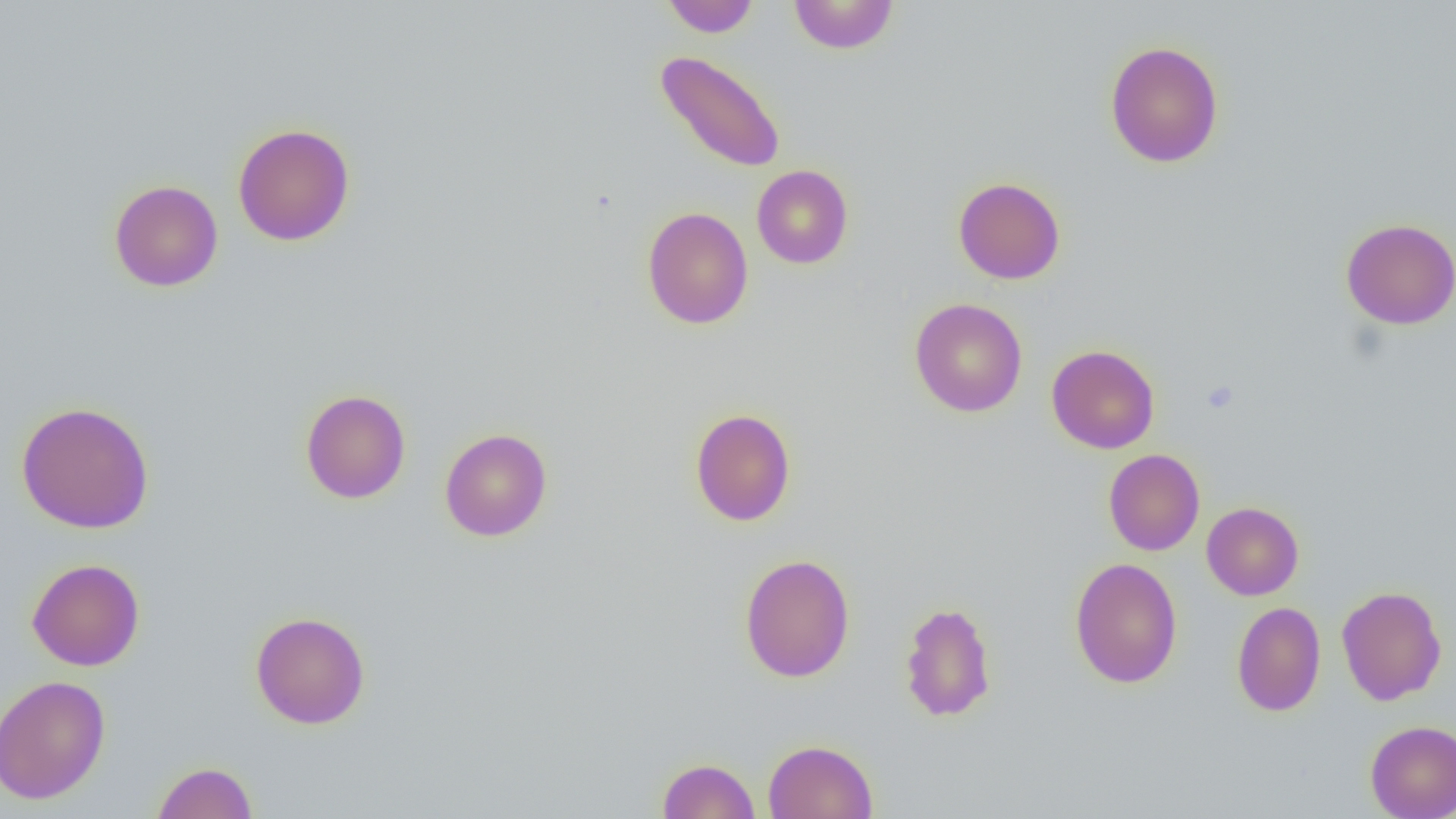 Approximate bounding boxes as named x1/y1/x2/y2 corners in pixels. Platelet locations: (x1=1201, y1=380, x2=1238, y2=413). Uninfected red blood cell locations: (x1=661, y1=0, x2=760, y2=37), (x1=788, y1=0, x2=900, y2=55), (x1=1104, y1=40, x2=1224, y2=168), (x1=654, y1=50, x2=786, y2=173), (x1=232, y1=123, x2=356, y2=246), (x1=751, y1=165, x2=853, y2=268), (x1=953, y1=177, x2=1066, y2=284), (x1=109, y1=179, x2=224, y2=292), (x1=641, y1=206, x2=754, y2=329), (x1=1340, y1=218, x2=1456, y2=330), (x1=909, y1=298, x2=1027, y2=417), (x1=1046, y1=344, x2=1160, y2=454), (x1=300, y1=389, x2=411, y2=504), (x1=16, y1=401, x2=155, y2=534), (x1=690, y1=408, x2=796, y2=527), (x1=439, y1=428, x2=552, y2=542), (x1=1103, y1=448, x2=1205, y2=555), (x1=1201, y1=501, x2=1304, y2=600), (x1=739, y1=552, x2=855, y2=683), (x1=1069, y1=557, x2=1183, y2=688), (x1=26, y1=558, x2=145, y2=671), (x1=1336, y1=585, x2=1447, y2=705), (x1=899, y1=600, x2=998, y2=722), (x1=1231, y1=601, x2=1326, y2=716), (x1=250, y1=611, x2=371, y2=729), (x1=0, y1=675, x2=111, y2=804), (x1=1365, y1=720, x2=1456, y2=818), (x1=763, y1=739, x2=878, y2=819), (x1=657, y1=758, x2=760, y2=818), (x1=151, y1=761, x2=258, y2=818). Slide-level diagnosis: no evidence of blood parasites. Thin blood film. Light microscopy. 1000x magnification. Image is 1456×819 pixels. Single field of view.